Point out each Plasmodium parasite.
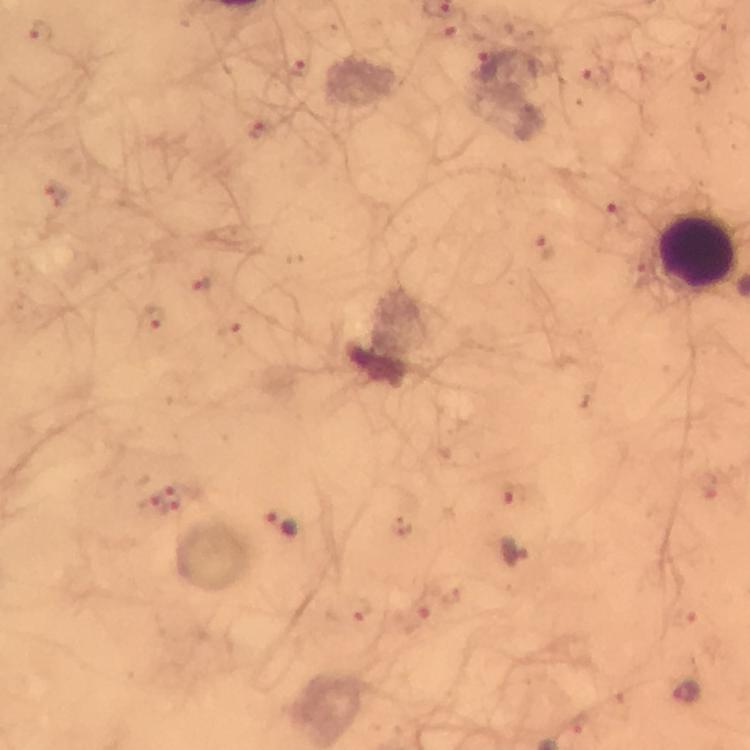
Approximate centers as {x, y} in pixels.
Plasmodium parasites: {452, 31}, {39, 33}, {488, 64}, {300, 68}, {592, 75}, {698, 83}, {261, 132}, {54, 196}, {615, 218}, {544, 246}, {199, 284}, {152, 317}, {230, 334}, {708, 484}, {182, 489}, {511, 495}, {151, 506}, {283, 525}, {516, 552}, {349, 611}, {684, 615}, {417, 623}, {685, 692}, {579, 726}.

magnification = 100x
image size = 750×750 pixels
leukocyte locations = approximate centers as {x, y} in pixels: {698, 251}
cropped from = a single field of view
context = from a diagnostic examination for malaria
stain = Giemsa
capture = smartphone camera through the microscope
immersion oil = used
preparation = thick blood smear